Locate every malaria parasite.
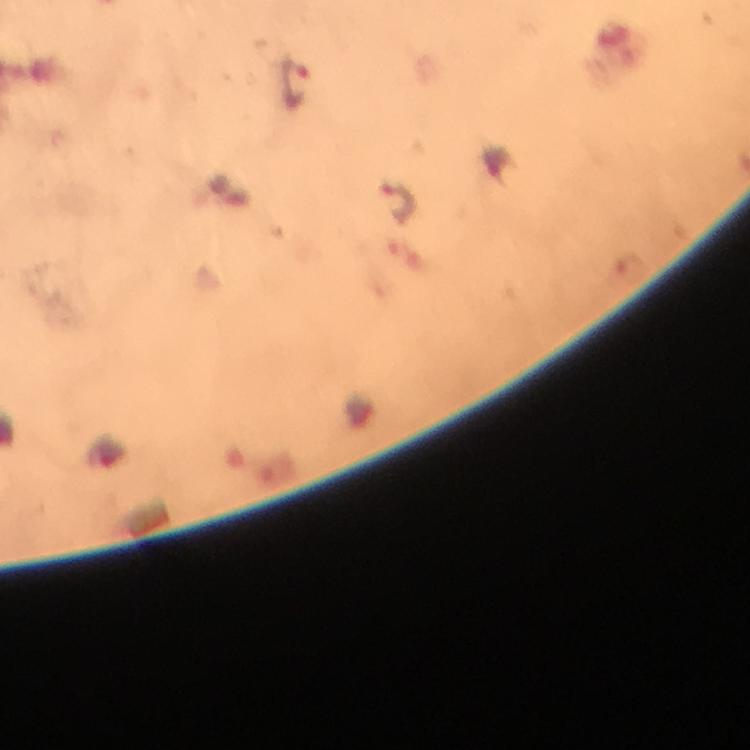
Approximate centers as {x, y} in pixels.
Malaria parasites: {294, 81}, {398, 202}.

Summary:
  - Magnification: 100x
  - Capture: smartphone mounted on the microscope
  - Immersion oil: applied
  - Cropped from: one field of view
  - Image size: 750×750 pixels
  - Context: from a diagnostic examination for malaria
  - Stain: Giemsa
  - Preparation: thick blood film